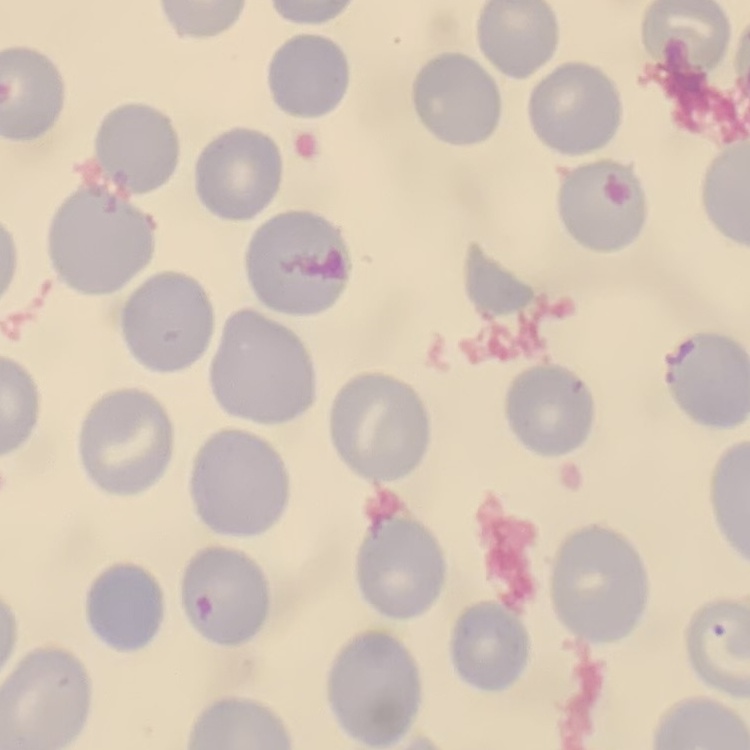

The erythrocytes show no rouleaux formation. Square crop of a larger photomicrograph. Thin peripheral smear. Stained with either Field's or Giemsa.